Assess the morphology of the erythrocytes.
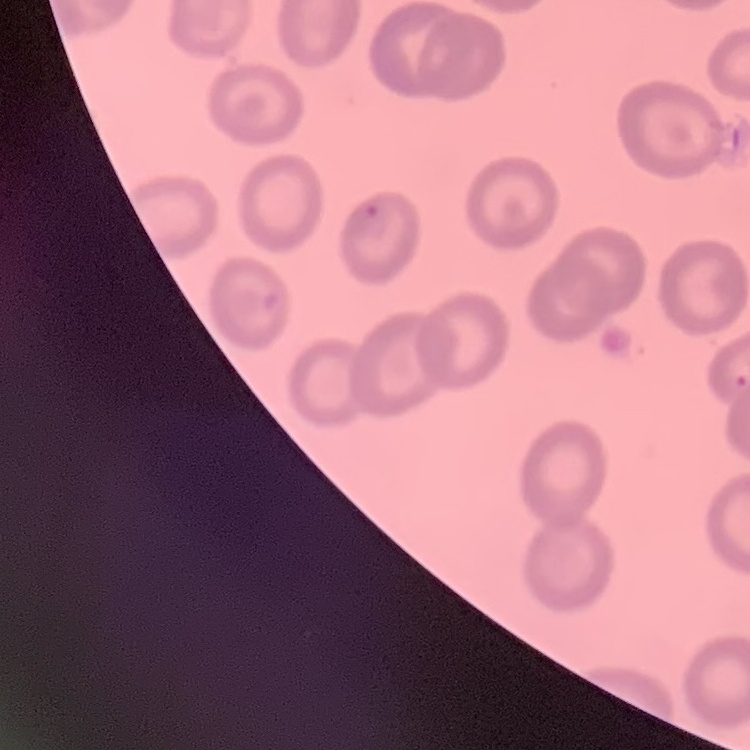

They show no rouleaux formation.

{
  "stain": "Field's or Giemsa",
  "preparation": "thin blood smear",
  "image_type": "square crop of a larger photomicrograph"
}